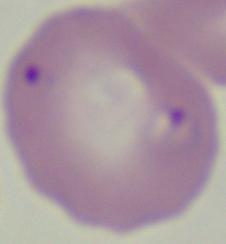 A Babesia parasite is seen. 1000x magnification. Micrograph.